Name the parasite shown.
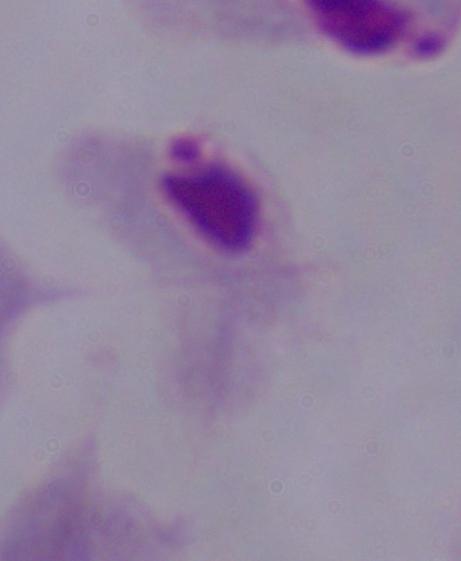

This is a trichomonad.

{
  "modality": "micrograph",
  "magnification": "1000x"
}